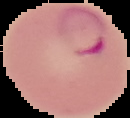
Summary:
  - Image size: 130×118 pixels
  - Preparation: thin blood film
  - Result: malaria parasites detected
  - Image type: segmented cell region with the area outside set to black